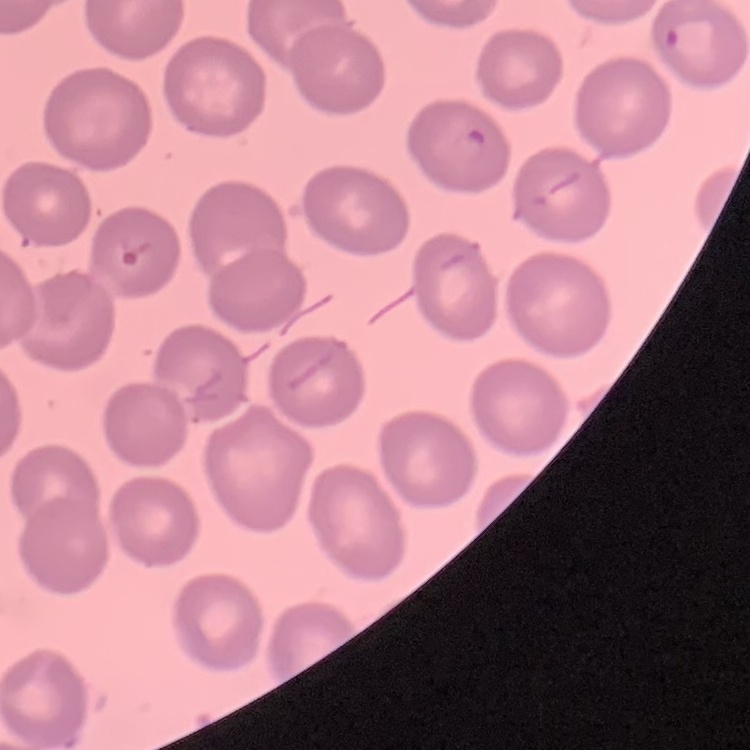 The red blood cells show no rouleaux formation. Thin peripheral smear. Square crop of a larger photomicrograph. Stained with either Field's or Giemsa.